Report the malaria status of this cell.
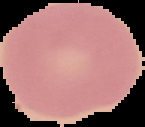
Uninfected.

Summary:
  - Preparation: thin blood film
  - Image size: 145×127 pixels
  - Image type: segmented cell region on a black background